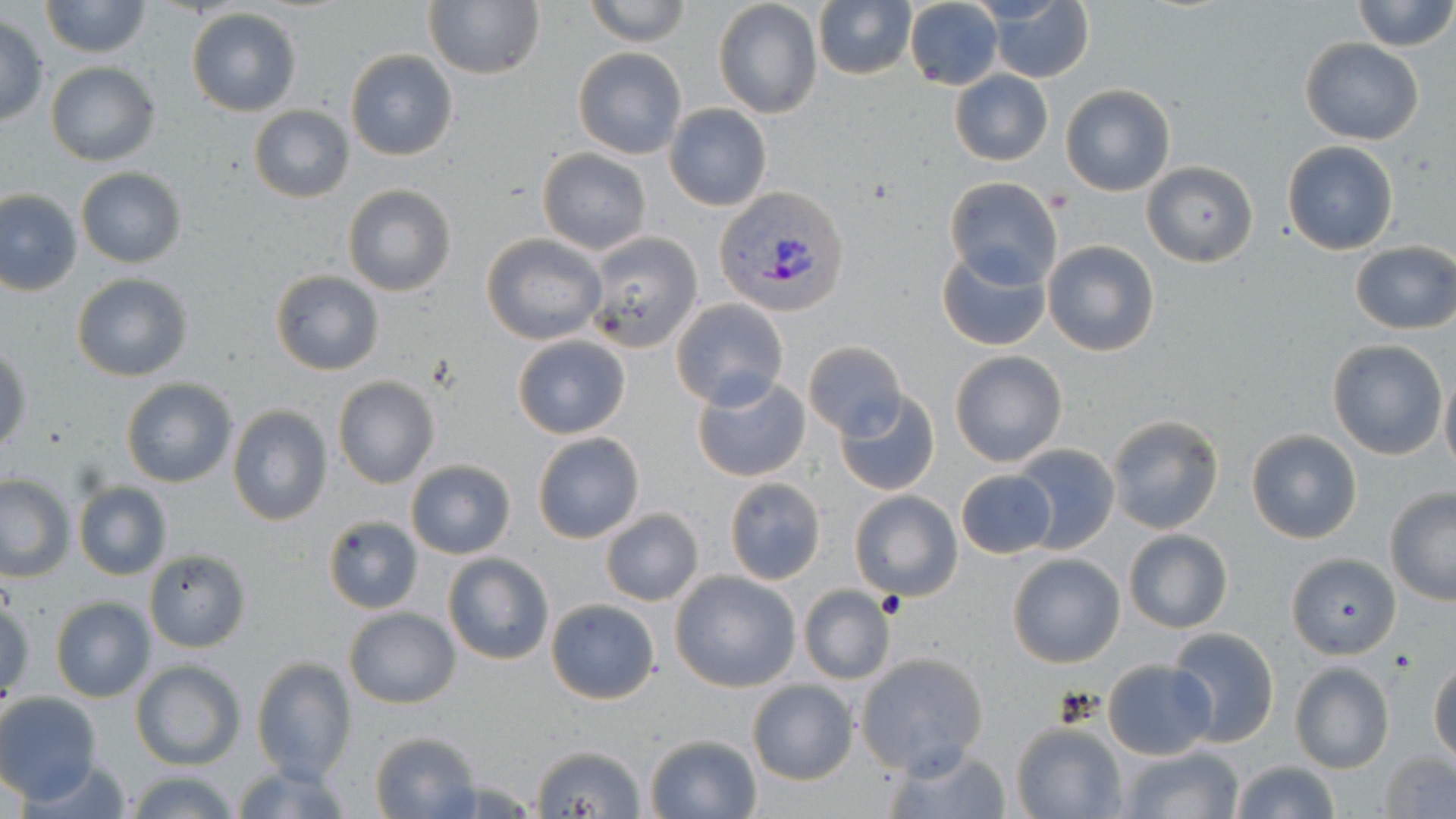 Approximate bounding boxes as (x1, y1, x2, y2) in pixels. Plasmodium vivax-infected red blood cell locations: (712, 187, 849, 319). Uninfected red blood cell locations: (39, 0, 150, 58), (583, 0, 689, 45), (812, 0, 918, 81), (904, 0, 1004, 91), (1350, 0, 1455, 51), (423, 1, 544, 81), (712, 1, 823, 119), (987, 2, 1094, 83), (186, 7, 302, 116), (0, 16, 47, 123), (1300, 38, 1423, 144), (572, 47, 687, 159), (345, 49, 458, 161), (44, 61, 161, 166), (950, 70, 1052, 165), (1060, 85, 1176, 197), (665, 104, 771, 211), (248, 105, 355, 202), (1282, 139, 1399, 255), (537, 147, 651, 255), (1141, 161, 1258, 268), (75, 167, 189, 269), (945, 177, 1062, 289), (342, 184, 457, 297), (1, 189, 82, 296), (584, 231, 703, 354), (481, 233, 607, 345), (1043, 240, 1159, 356), (1350, 242, 1456, 334), (937, 247, 1051, 351), (269, 269, 384, 376), (71, 273, 195, 383), (671, 300, 789, 411), (511, 336, 632, 438), (1327, 339, 1448, 460), (1, 342, 33, 454), (803, 342, 906, 437), (949, 349, 1069, 468), (1440, 369, 1456, 481), (691, 375, 812, 482), (332, 376, 440, 489), (120, 377, 237, 488), (834, 391, 940, 496), (226, 405, 333, 528), (1105, 414, 1226, 536), (1246, 428, 1363, 545), (532, 431, 645, 544), (1008, 443, 1119, 555), (405, 460, 515, 560), (954, 469, 1057, 560), (0, 474, 75, 582), (726, 476, 827, 584), (73, 482, 172, 581), (1384, 489, 1456, 604), (848, 490, 963, 603), (600, 508, 705, 606), (322, 515, 424, 614), (1124, 529, 1232, 632), (144, 549, 251, 652), (1285, 552, 1400, 659), (441, 553, 554, 667), (1007, 553, 1124, 668), (669, 571, 801, 693), (799, 585, 895, 685), (1, 596, 34, 703), (50, 598, 155, 703), (546, 598, 661, 705), (344, 608, 460, 709), (1165, 627, 1278, 747), (855, 652, 989, 774), (250, 656, 355, 784), (1102, 659, 1216, 759), (1429, 659, 1455, 763), (132, 661, 244, 769), (1289, 663, 1393, 774), (746, 680, 858, 785), (0, 692, 102, 804), (1010, 723, 1126, 818), (369, 730, 481, 818), (644, 734, 762, 818), (878, 741, 1012, 819), (526, 742, 651, 819), (1118, 745, 1243, 819), (1378, 749, 1456, 818), (18, 760, 139, 817), (1228, 760, 1340, 819), (233, 761, 352, 819), (126, 768, 241, 819). Platelet locations: (875, 593, 907, 620), (1386, 647, 1421, 680). Slide-level diagnosis: Plasmodium vivax. Optical microscopy. Thin blood film. May-Grünwald-Giemsa-stained preparation. Captured at 1000x magnification. One field of a larger specimen. Image is 1456×819 pixels.